Name the blood parasite species.
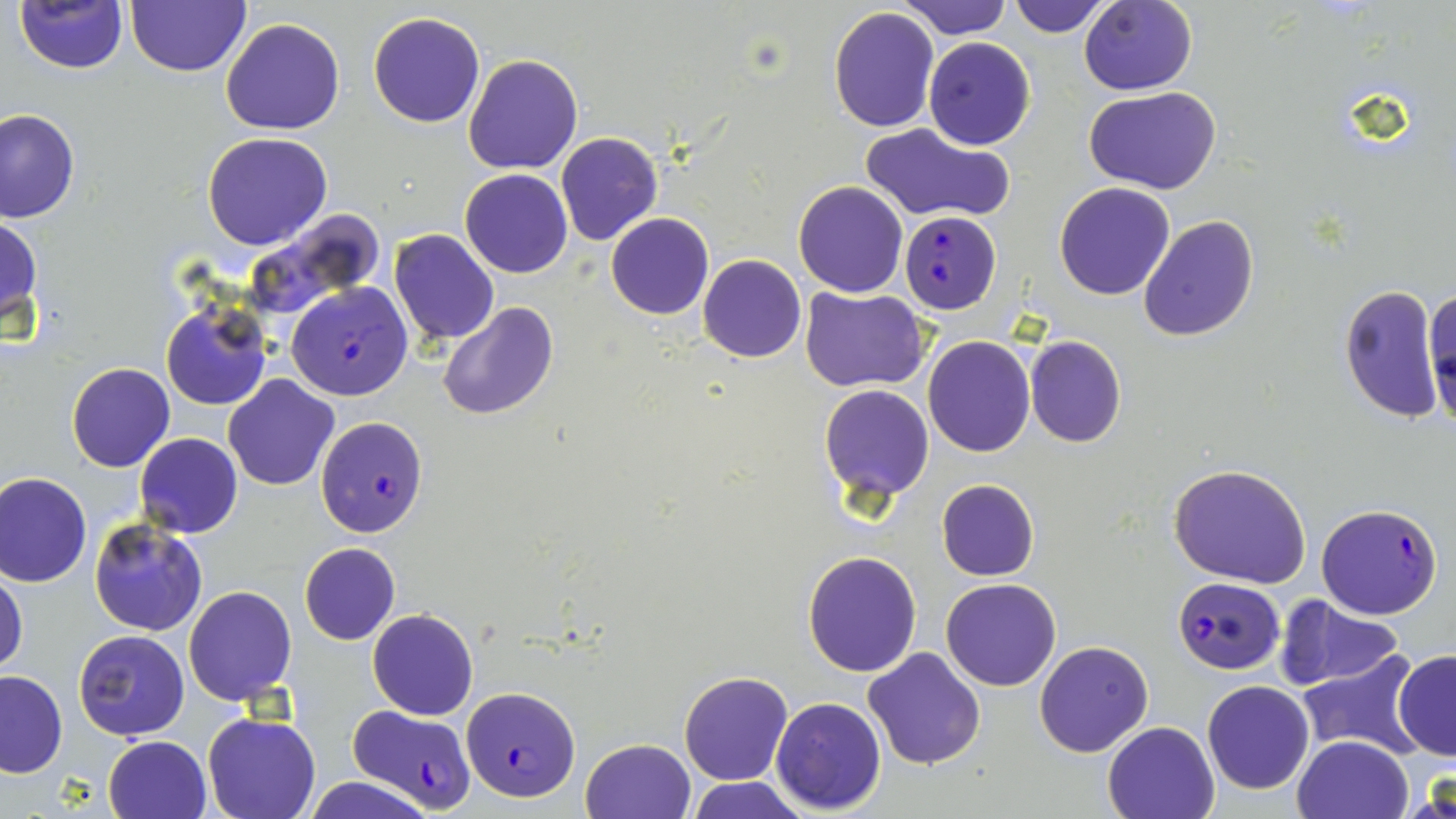

Plasmodium falciparum.

preparation = thin blood film
modality = optical microscopy
field of view = single
magnification = 1000x
uninfected red blood cell locations = approximate bounding boxes as [x1, y1, x2, y2] in pixels: [13, 0, 127, 73], [125, 0, 251, 77], [897, 0, 1012, 40], [1007, 0, 1115, 37], [1079, 0, 1198, 95], [827, 8, 941, 131], [368, 11, 487, 128], [221, 18, 345, 135], [923, 37, 1035, 151], [462, 54, 583, 173], [1085, 86, 1222, 195], [0, 108, 80, 222], [859, 121, 1010, 223], [202, 133, 332, 250], [555, 133, 662, 246], [460, 169, 573, 278], [793, 181, 908, 297], [1054, 183, 1175, 300], [239, 211, 389, 321], [606, 212, 713, 320], [0, 213, 43, 337], [1138, 214, 1260, 342], [389, 230, 498, 345], [697, 254, 806, 363], [1337, 285, 1445, 421], [1425, 287, 1456, 422], [800, 288, 929, 392], [438, 301, 559, 421], [161, 302, 272, 411], [1024, 335, 1127, 448], [922, 336, 1035, 456], [66, 361, 174, 472], [224, 375, 341, 491], [819, 384, 934, 502], [135, 433, 243, 539], [1168, 462, 1314, 589], [0, 471, 92, 587], [936, 479, 1039, 581], [89, 517, 208, 637], [299, 542, 400, 645], [803, 552, 922, 676], [0, 565, 28, 678], [941, 577, 1064, 691], [183, 584, 297, 704], [1275, 597, 1405, 690], [367, 609, 478, 720], [74, 629, 189, 740], [1033, 640, 1153, 757], [862, 646, 985, 769], [1392, 649, 1456, 761], [1296, 653, 1423, 760], [0, 669, 67, 777], [679, 670, 793, 785], [1202, 680, 1315, 794], [770, 696, 887, 815], [203, 711, 321, 818], [1101, 720, 1221, 818], [103, 735, 212, 819], [1292, 735, 1415, 819], [580, 738, 696, 819], [1407, 767, 1456, 819], [301, 774, 438, 819], [685, 776, 811, 819]
image size = 1456×819 pixels
Plasmodium falciparum-infected red blood cell locations = approximate bounding boxes as [x1, y1, x2, y2] in pixels: [901, 209, 1001, 313], [286, 282, 414, 401], [314, 416, 428, 537], [1316, 501, 1443, 619], [1173, 577, 1284, 674], [461, 685, 581, 801], [346, 703, 480, 811]
stain = May-Grünwald-Giemsa